Outline each blood parasite and name the species.
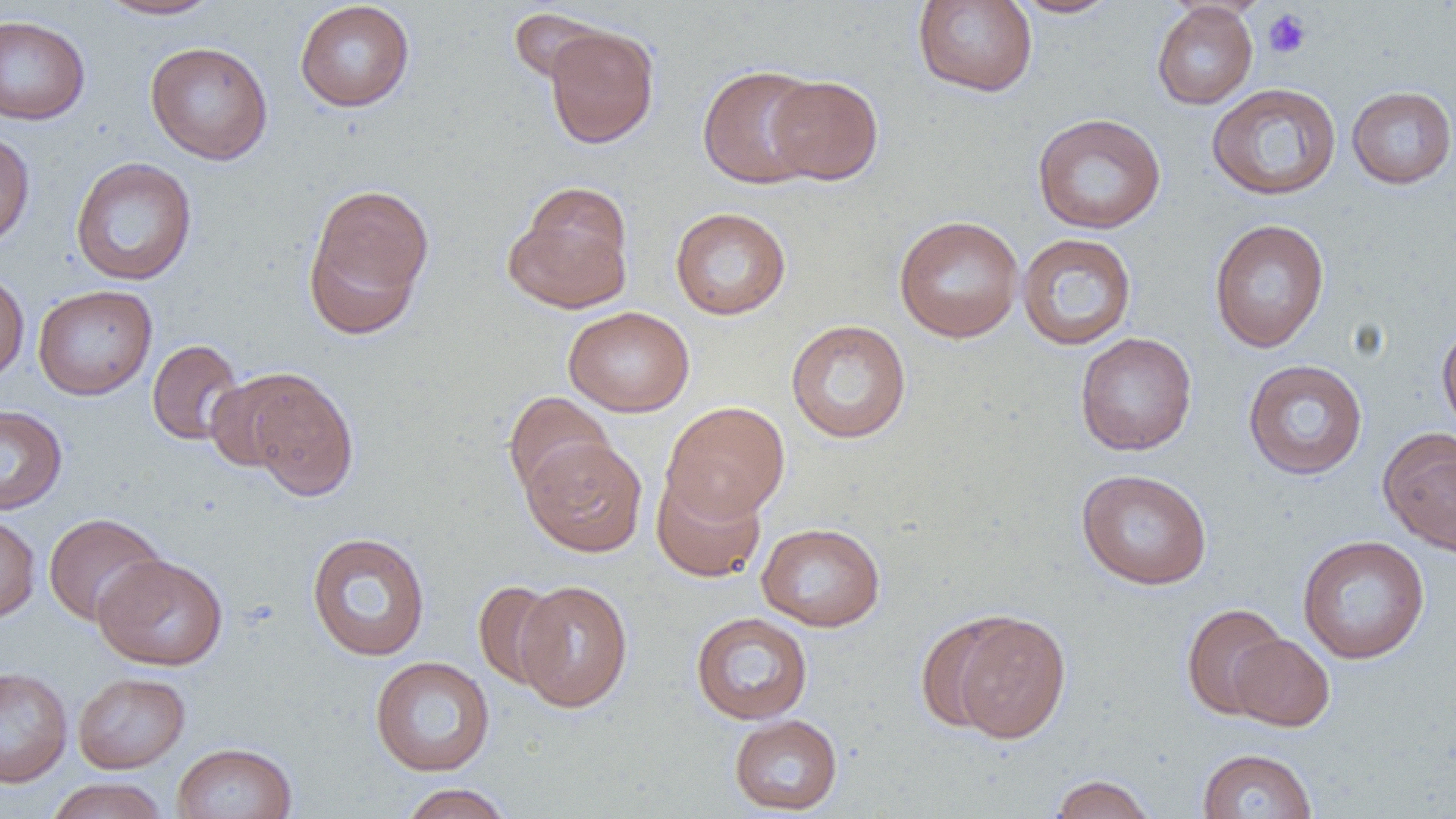

No blood parasites observed.

Summary:
  - Coordinate format: approximate bounding boxes as [x1, y1, x2, y2] in pixels
  - Platelet locations: [1263, 9, 1312, 59]
  - Uninfected red blood cell locations: [95, 0, 224, 20], [912, 0, 1038, 97], [1008, 0, 1122, 18], [294, 1, 415, 112], [1151, 3, 1258, 109], [507, 7, 611, 86], [0, 15, 91, 125], [544, 23, 659, 149], [145, 41, 273, 164], [697, 64, 824, 189], [766, 74, 884, 185], [1206, 82, 1341, 201], [1346, 86, 1456, 188], [1032, 113, 1166, 234], [0, 129, 35, 251], [70, 157, 198, 286], [304, 182, 435, 333], [507, 186, 634, 312], [670, 207, 792, 320], [894, 215, 1024, 342], [1208, 219, 1330, 353], [1016, 232, 1137, 350], [0, 268, 29, 385], [32, 284, 158, 400], [563, 306, 695, 417], [785, 319, 912, 444], [1436, 320, 1456, 439], [1075, 332, 1197, 456], [147, 338, 245, 445], [1242, 359, 1368, 480], [204, 370, 313, 472], [245, 372, 359, 501], [503, 391, 614, 499], [661, 401, 790, 521], [0, 404, 67, 515], [1378, 426, 1456, 556], [522, 437, 648, 556], [1075, 468, 1213, 590], [651, 470, 766, 583], [0, 512, 40, 623], [43, 513, 167, 626], [756, 522, 886, 631], [306, 531, 431, 661], [1297, 534, 1430, 664], [92, 553, 229, 670], [473, 580, 565, 689], [514, 580, 633, 712], [1181, 602, 1289, 719], [946, 611, 1072, 742], [690, 612, 813, 725], [1228, 633, 1334, 731], [369, 656, 496, 776], [0, 666, 73, 788], [72, 671, 190, 773], [729, 713, 843, 815], [172, 742, 297, 819], [1197, 748, 1318, 819], [1048, 774, 1157, 819], [44, 777, 169, 819], [397, 783, 515, 819]
  - Slide-level diagnosis: no evidence of blood parasites
  - Image size: 1456×819 pixels
  - Preparation: thin blood smear
  - Field of view: single
  - Modality: optical microscopy
  - Magnification: 1000x